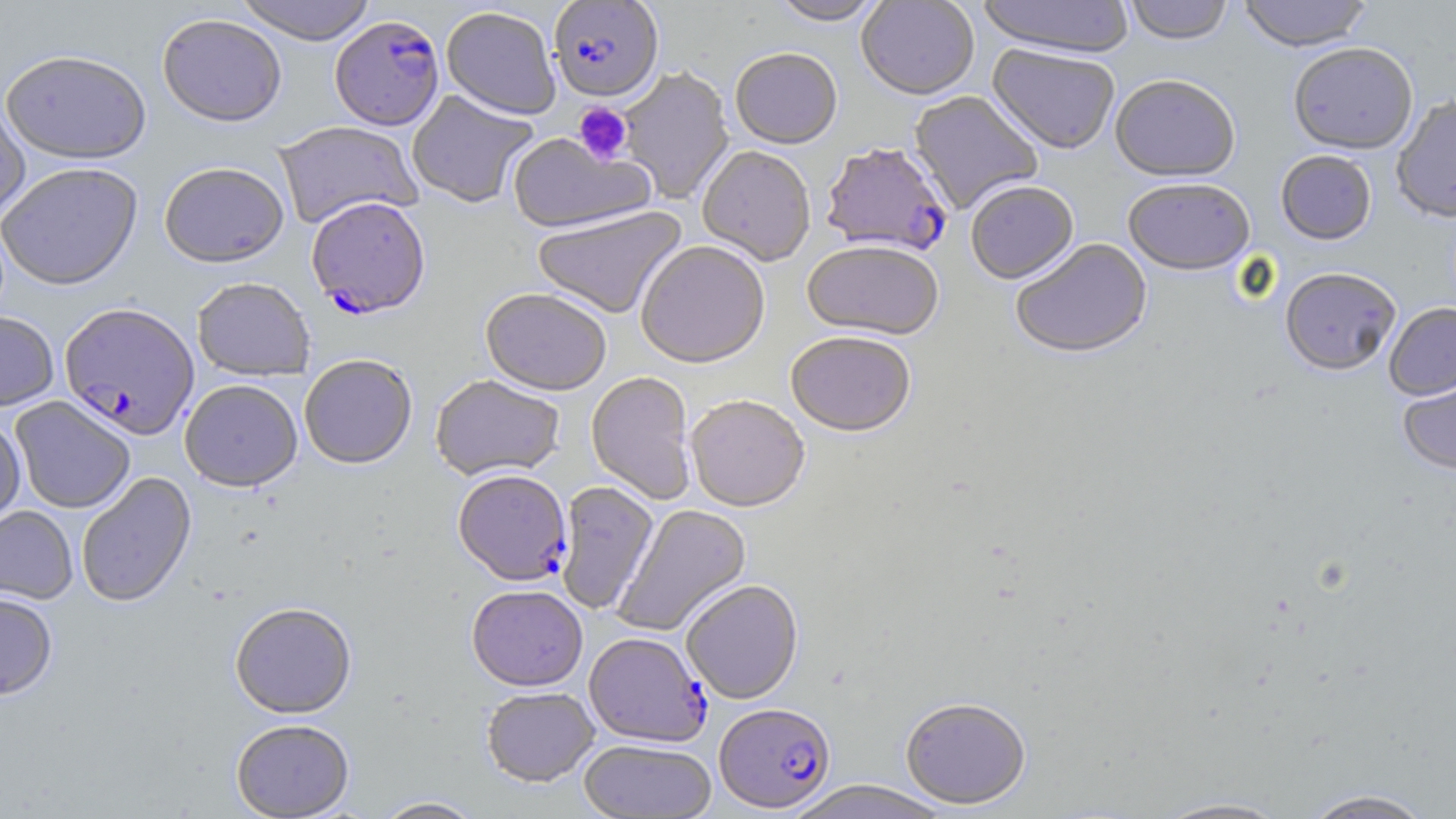
Approximate bounding boxes as [x1, y1, x2, y2] in pixels. Uninfected red blood cell locations: [233, 0, 378, 47], [769, 0, 886, 28], [856, 0, 979, 102], [977, 0, 1136, 60], [1123, 0, 1234, 46], [1237, 0, 1373, 52], [441, 8, 560, 123], [157, 16, 287, 131], [1288, 42, 1418, 155], [987, 45, 1120, 157], [730, 51, 842, 151], [1, 54, 151, 167], [618, 67, 735, 205], [1110, 75, 1241, 184], [407, 91, 538, 208], [908, 91, 1043, 215], [1391, 96, 1456, 224], [0, 103, 30, 223], [273, 123, 423, 231], [507, 134, 656, 237], [697, 148, 816, 268], [1276, 150, 1377, 245], [0, 165, 143, 293], [159, 165, 289, 270], [1123, 179, 1255, 278], [966, 183, 1079, 287], [532, 206, 689, 320], [1011, 240, 1152, 361], [635, 242, 771, 371], [802, 244, 943, 342], [1280, 267, 1401, 377], [192, 280, 315, 383], [480, 290, 610, 399], [1384, 302, 1456, 401], [0, 313, 59, 412], [786, 334, 915, 440], [300, 357, 417, 471], [1397, 366, 1456, 476], [586, 372, 696, 506], [430, 376, 565, 483], [180, 382, 302, 495], [10, 397, 135, 514], [686, 397, 809, 515], [0, 419, 25, 527], [77, 473, 197, 609], [555, 482, 660, 616], [613, 504, 753, 637], [0, 506, 78, 605], [682, 581, 804, 705], [466, 587, 588, 693], [0, 593, 58, 704], [230, 604, 357, 721], [481, 689, 599, 789], [900, 699, 1031, 811], [232, 722, 354, 819], [579, 740, 718, 818], [782, 781, 951, 818], [1300, 789, 1436, 818], [1151, 796, 1293, 818], [371, 797, 486, 818]. Plasmodium falciparum-infected red blood cell locations: [549, 1, 664, 104], [330, 18, 444, 133], [821, 145, 953, 260], [306, 200, 431, 322], [60, 305, 200, 443], [453, 472, 571, 588], [584, 633, 711, 748], [713, 705, 835, 815]. Platelet locations: [573, 102, 634, 166]. Slide-level diagnosis: Plasmodium falciparum. 1000x magnification. Image is 1456×819 pixels. May-Grünwald-Giemsa stain. Optical microscopy. Single field of view. Thin blood film.